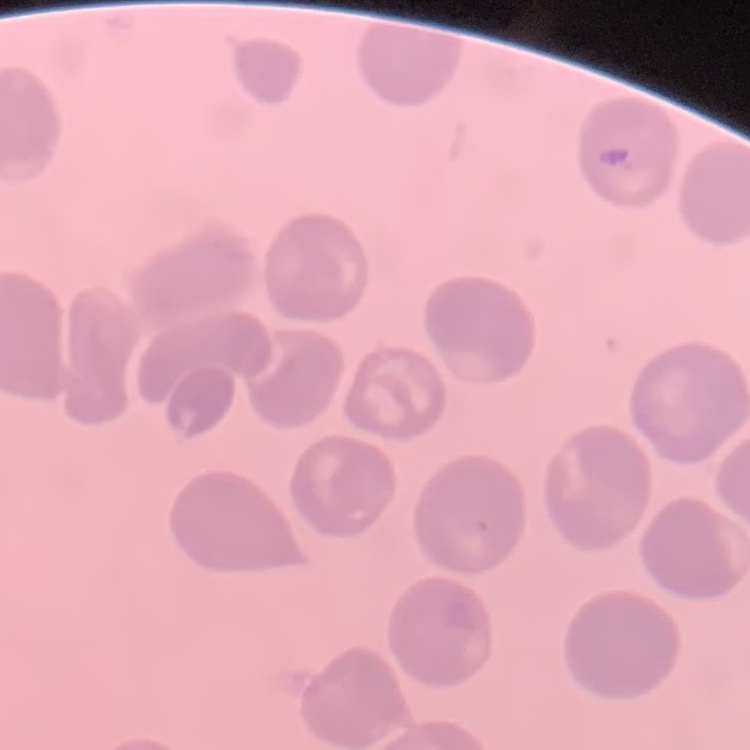

Summary:
  - Erythrocyte morphology: no rouleaux formation
  - Stain: Field's or Giemsa
  - Image type: square crop of a larger photomicrograph
  - Preparation: thin blood film